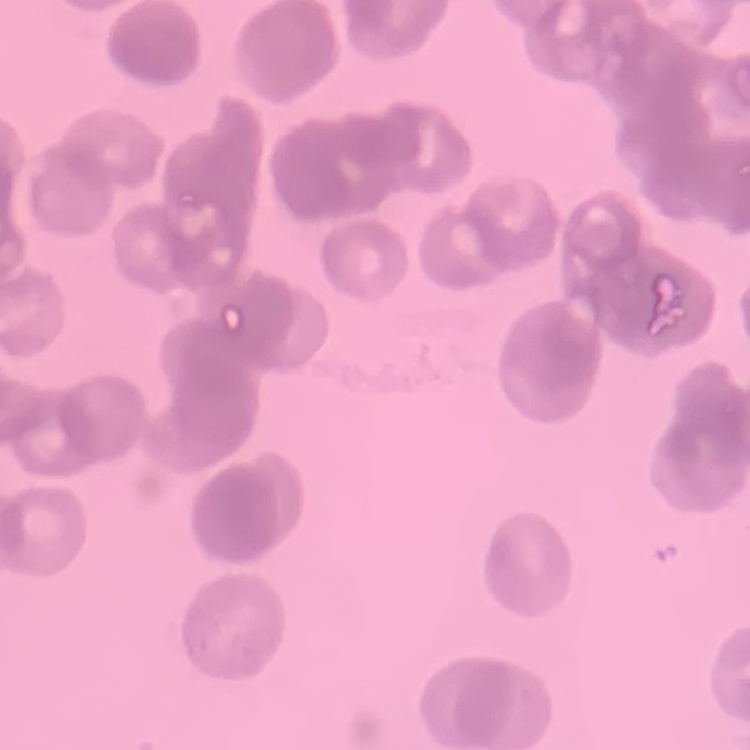

The erythrocytes show rouleaux formation. One tile cut from a larger photomicrograph. Stained with either Field's or Giemsa. Thin peripheral smear.